Report the malaria status of this cell.
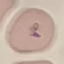
It is uninfected.

{
  "capture": "smartphone camera at the microscope eyepiece",
  "preparation": "thin blood smear",
  "stain": "Giemsa",
  "image_type": "automatically extracted cell patch, resized to 64 × 64 pixels"
}